Give the position of every leukocyte visible.
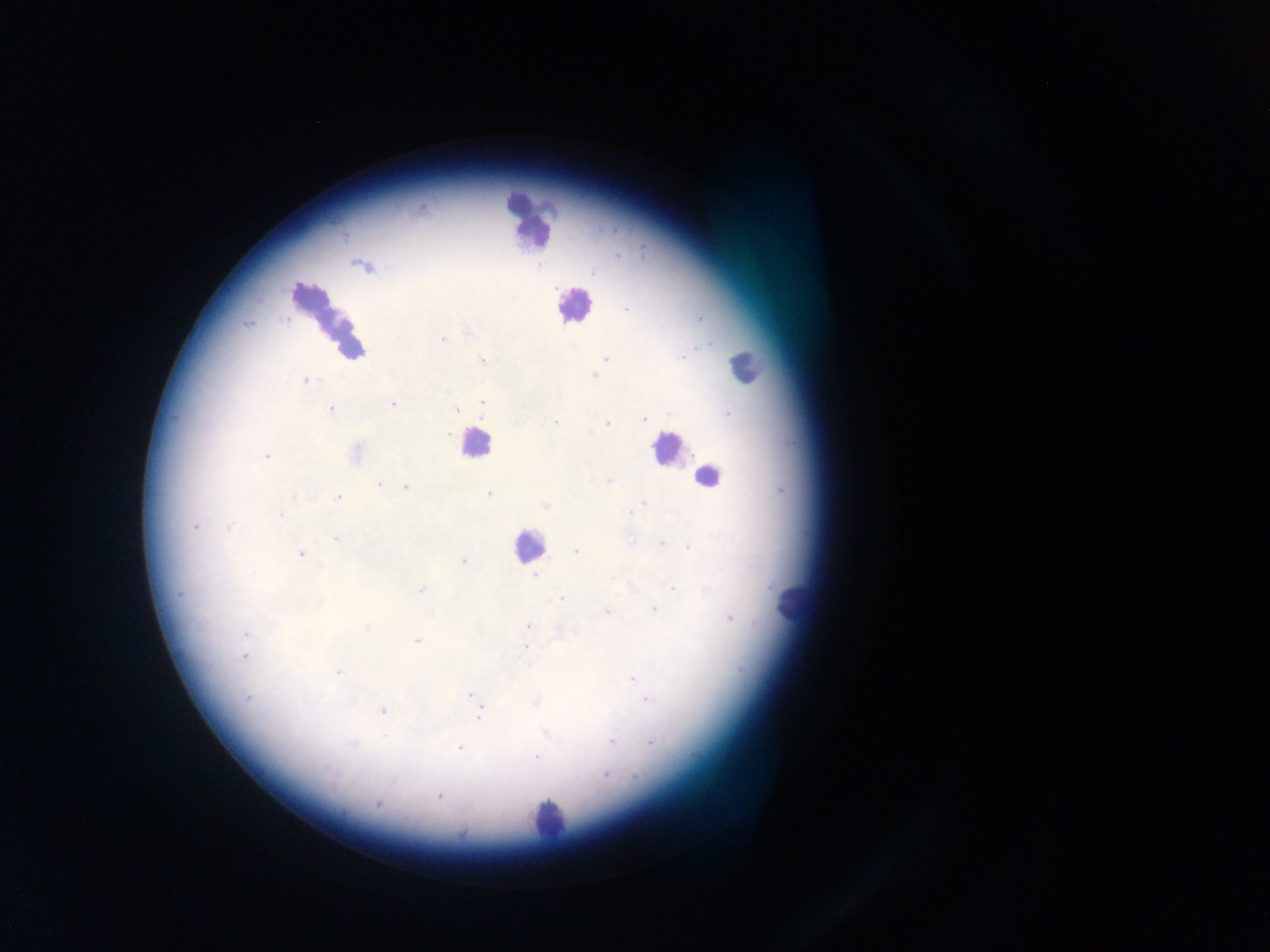
Approximate centers as [x, y] in pixels.
Leukocytes: [529, 222], [573, 305], [329, 321], [745, 367], [475, 443], [666, 447], [708, 476], [528, 547], [792, 604], [548, 820].

capture = mobile-phone photograph through a microscope
preparation = thick blood film
Plasmodium parasite locations = approximate centers as [x, y] in pixels: [363, 266], [592, 271], [443, 339], [606, 359], [481, 360], [305, 379], [482, 401], [393, 404], [456, 408], [330, 409], [644, 418], [556, 422], [606, 422], [356, 453], [265, 456], [608, 480], [379, 483], [406, 486], [489, 495], [337, 497], [544, 505], [631, 512], [194, 527], [337, 538], [661, 544], [689, 546], [575, 551], [300, 552], [463, 561], [536, 576], [673, 588], [422, 589], [561, 598], [655, 610], [606, 612], [730, 618], [529, 626], [561, 630], [245, 634], [417, 640], [525, 646], [244, 656], [337, 671], [631, 678], [472, 693], [647, 701], [383, 709], [480, 712], [612, 741], [460, 748], [535, 756], [608, 774], [440, 796], [377, 804]
country = Ghana
image size = 1270×952 pixels
field of view = single